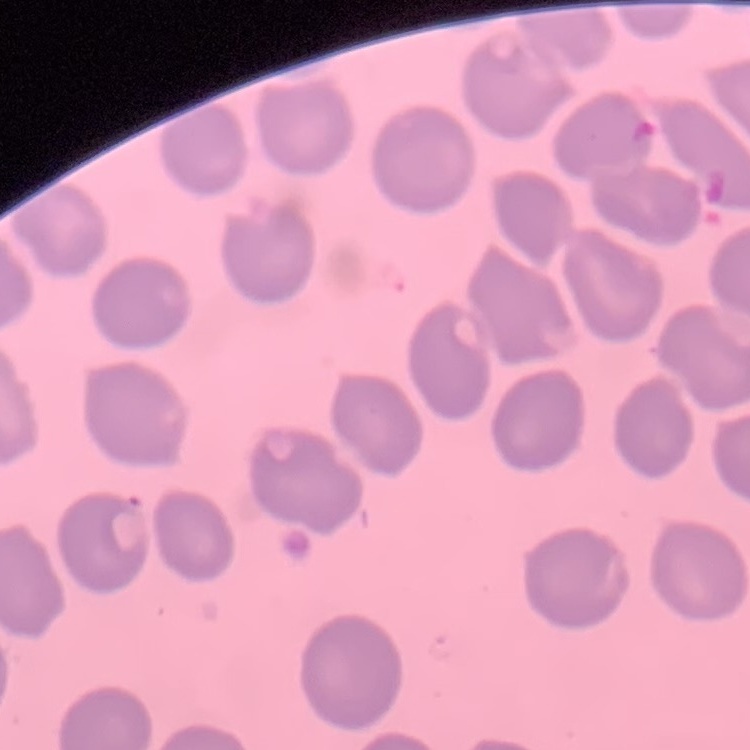

Summary:
  - Red blood cell morphology: no rouleaux formation
  - Stain: Field's or Giemsa
  - Preparation: thin blood smear
  - Image type: one tile cut from a larger photomicrograph